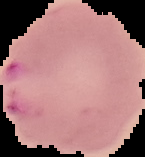

Summary:
  - Preparation: thin blood film
  - Result: Plasmodium parasites identified
  - Image size: 145×157 pixels
  - Image type: segmented cell region on a black background